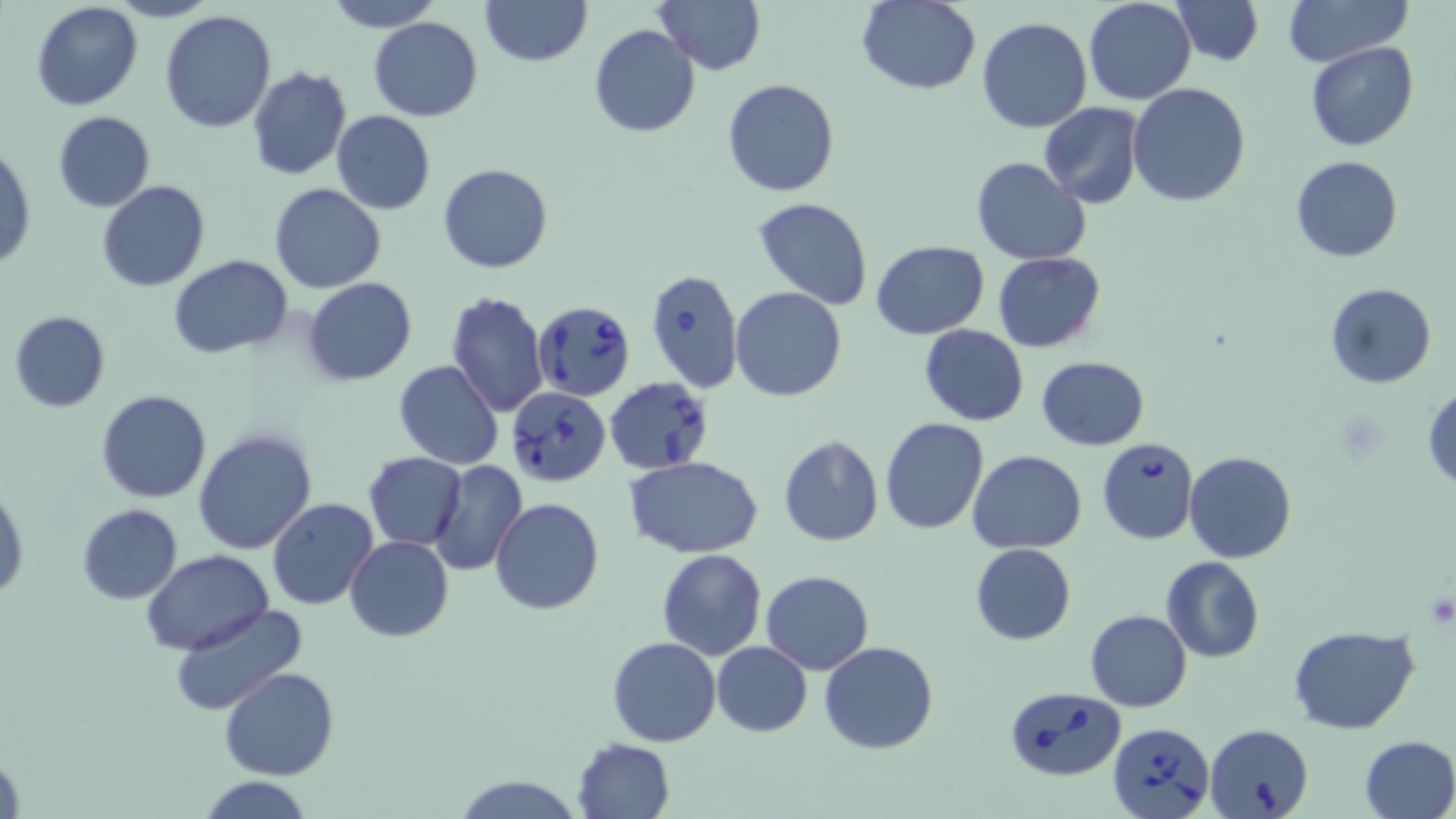

slide-level diagnosis = Babesia divergens
uninfected red blood cell locations = approximate bounding boxes as (x1, y1, x2, y2) in pixels: (324, 0, 442, 32), (480, 0, 591, 67), (653, 0, 765, 75), (1082, 0, 1197, 105), (1170, 0, 1263, 66), (1282, 0, 1413, 66), (31, 1, 143, 111), (858, 1, 982, 95), (159, 10, 276, 133), (369, 17, 483, 122), (976, 17, 1092, 133), (589, 24, 700, 139), (1304, 40, 1419, 151), (247, 68, 351, 181), (722, 78, 841, 198), (1127, 83, 1251, 206), (1040, 104, 1143, 208), (52, 110, 156, 212), (331, 110, 435, 214), (1, 142, 35, 271), (1289, 155, 1403, 263), (972, 157, 1091, 266), (437, 163, 554, 274), (95, 180, 211, 291), (269, 184, 386, 294), (754, 196, 873, 308), (870, 240, 990, 340), (993, 252, 1105, 352), (167, 254, 293, 358), (302, 278, 416, 386), (1325, 282, 1435, 387), (730, 287, 847, 401), (445, 290, 549, 419), (8, 310, 110, 413), (920, 324, 1029, 426), (1037, 356, 1149, 451), (394, 360, 504, 471), (1424, 386, 1456, 490), (132, 387, 280, 529), (97, 390, 212, 504), (880, 416, 989, 534), (192, 429, 317, 556), (777, 435, 884, 547), (970, 450, 1087, 554), (1185, 451, 1297, 563), (363, 452, 467, 549), (624, 457, 766, 559), (429, 459, 528, 577), (1, 483, 28, 603), (266, 497, 379, 610), (488, 497, 604, 614), (76, 504, 183, 604), (345, 535, 452, 641), (971, 543, 1075, 645), (656, 549, 767, 660), (142, 550, 274, 655), (1161, 556, 1263, 663), (760, 570, 874, 674), (168, 603, 308, 716), (1086, 610, 1192, 711), (1288, 625, 1420, 733), (607, 636, 721, 746), (820, 640, 939, 753), (711, 642, 813, 737), (221, 667, 339, 781), (1358, 735, 1456, 819), (572, 738, 676, 819), (454, 774, 582, 818), (197, 777, 314, 818)
modality = light microscopy
magnification = 1000x
stain = May-Grünwald-Giemsa
image size = 1456×819 pixels
platelet locations = approximate bounding boxes as (x1, y1, x2, y2) in pixels: (1424, 594, 1454, 628)
Babesia divergens-infected red blood cell locations = approximate bounding boxes as (x1, y1, x2, y2) in pixels: (646, 268, 744, 393), (533, 300, 636, 400), (604, 377, 715, 474), (507, 386, 610, 486), (1097, 437, 1200, 545), (1002, 685, 1125, 782), (1106, 720, 1217, 818), (1205, 722, 1314, 819)
field of view = single
preparation = thin blood film